Locate every uninfected red blood cell.
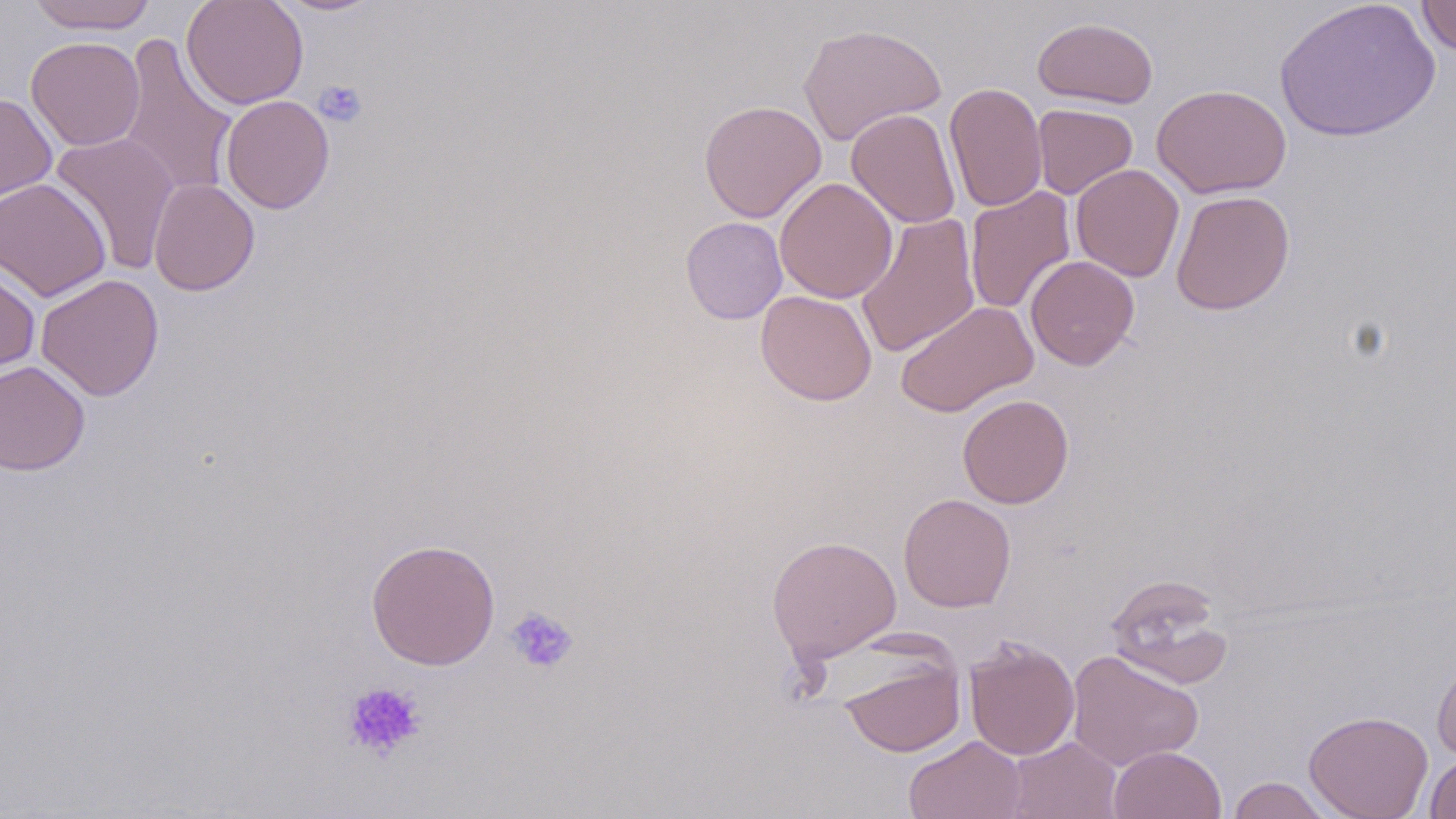
Approximate bounding boxes as (x1,y1)-(x2,y2) corner pairs in pixels.
Uninfected red blood cells: (26,0)-(158,34), (181,0)-(309,110), (273,0)-(383,16), (1274,0)-(1440,143), (1416,0)-(1456,57), (1033,16)-(1158,109), (798,23)-(946,146), (118,35)-(238,199), (26,36)-(145,151), (944,82)-(1047,213), (1152,84)-(1291,198), (0,92)-(57,202), (221,95)-(335,214), (698,99)-(826,223), (1032,103)-(1138,199), (846,108)-(962,228), (50,131)-(181,273), (1070,163)-(1184,281), (0,177)-(111,301), (774,177)-(898,303), (148,178)-(260,296), (965,186)-(1076,315), (1171,190)-(1295,315), (855,212)-(981,358), (680,216)-(788,324), (1025,254)-(1140,370), (0,261)-(41,375), (35,273)-(165,401), (755,290)-(877,405), (895,301)-(1038,418), (0,360)-(91,476), (958,394)-(1074,508), (898,494)-(1016,613), (766,535)-(902,664), (366,538)-(501,670), (1105,574)-(1233,689), (963,635)-(1080,761), (1431,648)-(1456,761), (837,650)-(966,758), (1066,650)-(1204,772), (1303,710)-(1433,819), (904,735)-(1026,819), (1007,736)-(1122,819), (1108,746)-(1227,819), (1425,752)-(1456,818), (1227,776)-(1335,818).

Platelet locations: (313,79)-(368,128), (505,606)-(579,675), (341,681)-(427,761). Slide-level diagnosis: negative for blood parasites. Captured at 1000x magnification. Image is 1456×819 pixels. Single field of view. May-Grünwald-Giemsa-stained preparation. Light microscopy. Thin blood smear.